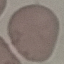
Summary:
  - Malaria status: uninfected
  - Image type: automatically extracted cell patch, resized to 64 × 64 pixels
  - Capture: smartphone camera at the microscope eyepiece
  - Preparation: thin blood film
  - Stain: Giemsa